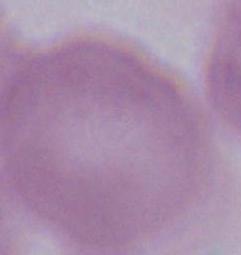

Summary:
  - Identification: red blood cell
  - Modality: micrograph
  - Magnification: 1000x